Name the parasite shown.
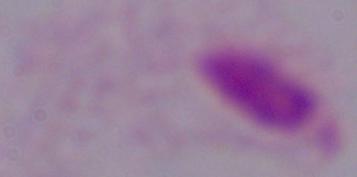
This is a trichomonad.

Photomicrograph. Captured at 1000x magnification.